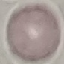 Malaria status: uninfected. Thin smear of blood. Automatically extracted cell patch, resized to 64 × 64 pixels. Giemsa stain. Photographed with a smartphone camera at the microscope eyepiece.